Look for Plasmodium parasites.
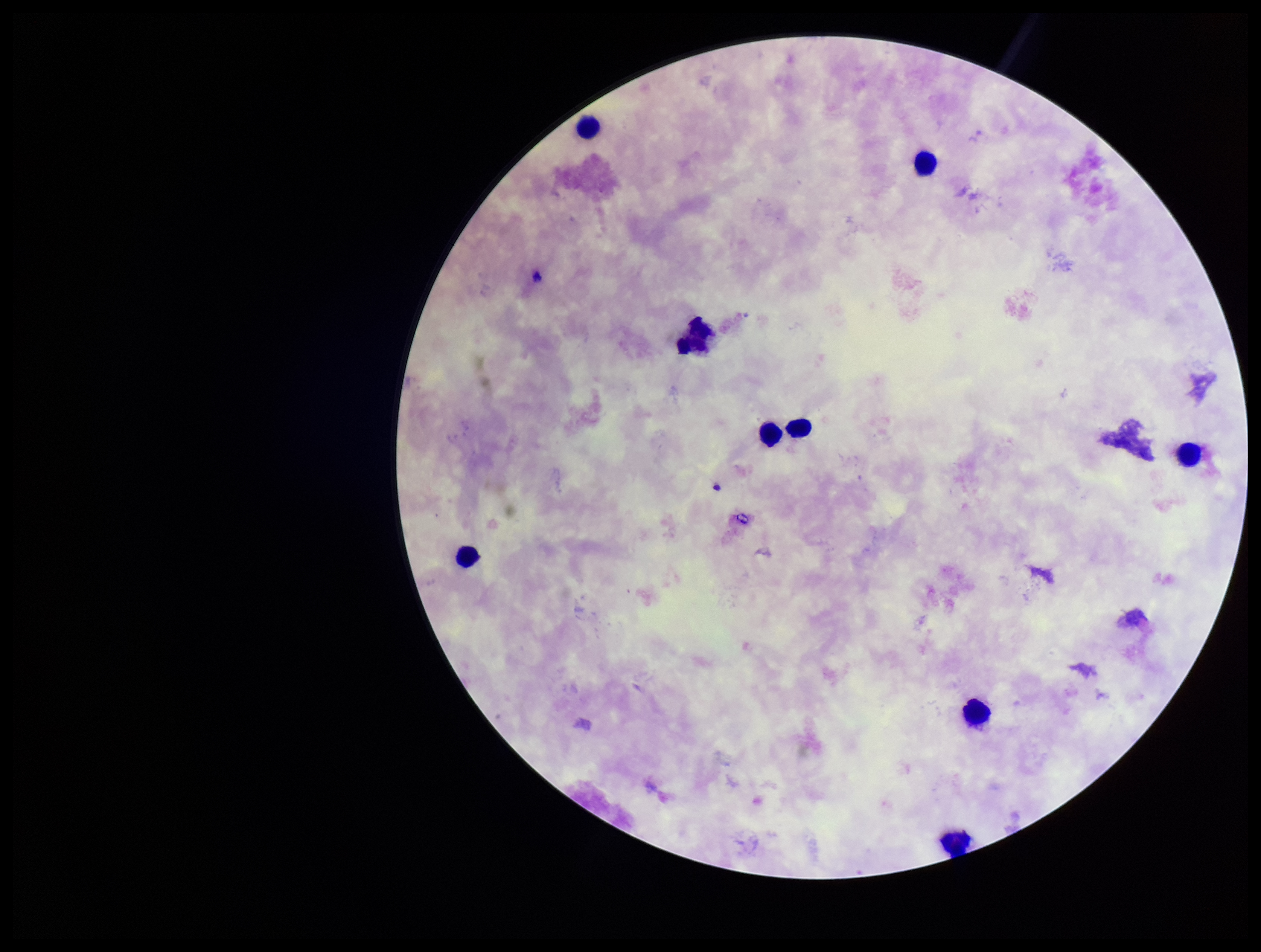

None identified.

Summary:
  - Patient malaria status: negative
  - Capture: smartphone photograph through the microscope eyepiece
  - Parasite count: 0
  - Stain: Giemsa
  - Preparation: thick blood smear
  - Leukocyte count: 9
  - Field of view: single
  - Image size: 1261×952 pixels